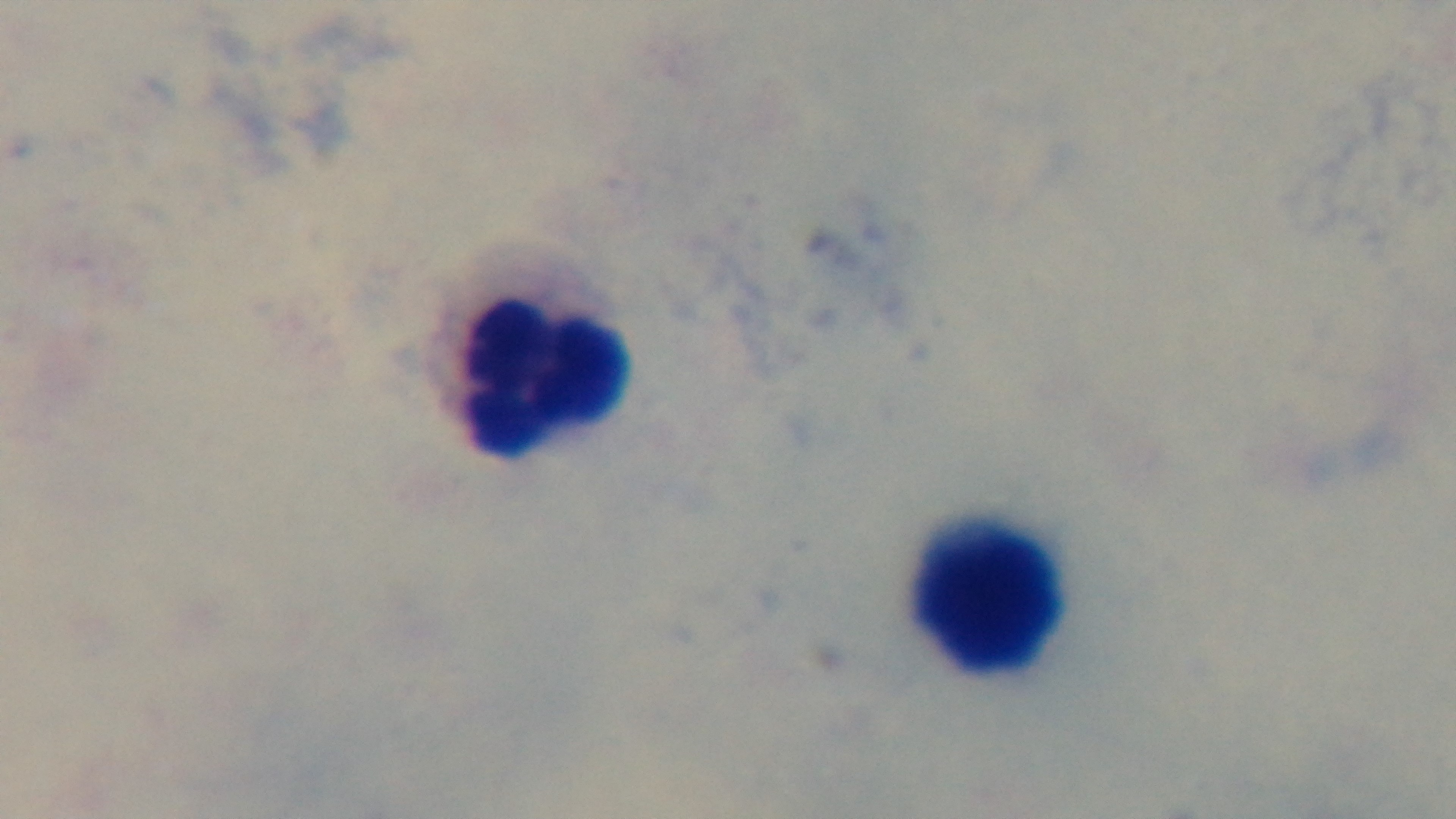

Summary:
  - Stain: Giemsa
  - Malaria status: uninfected
  - Field of view: one from the slide
  - Modality: light microscopy
  - Preparation: thick smear
  - Objective: 100x oil immersion
  - Capture: mounted 4K digital camera